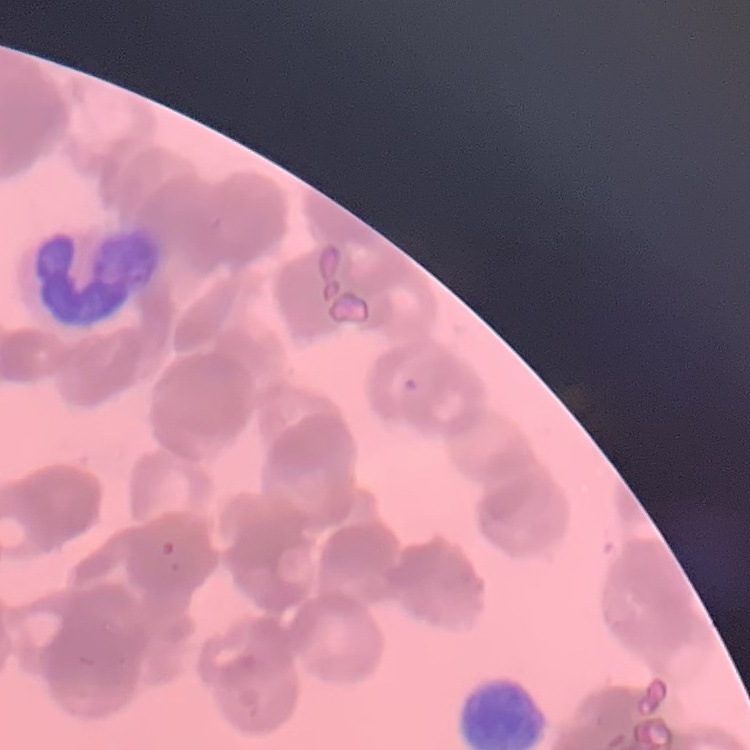
The erythrocytes exhibit rouleaux formation. Square crop of a larger photomicrograph. Stained with either Field's or Giemsa. Thin blood film.